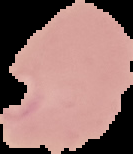 Segmented cell region on a black background. Image is 133×154 pixels. Result: Plasmodium parasites detected. From a thin blood film.